State the preparation type.
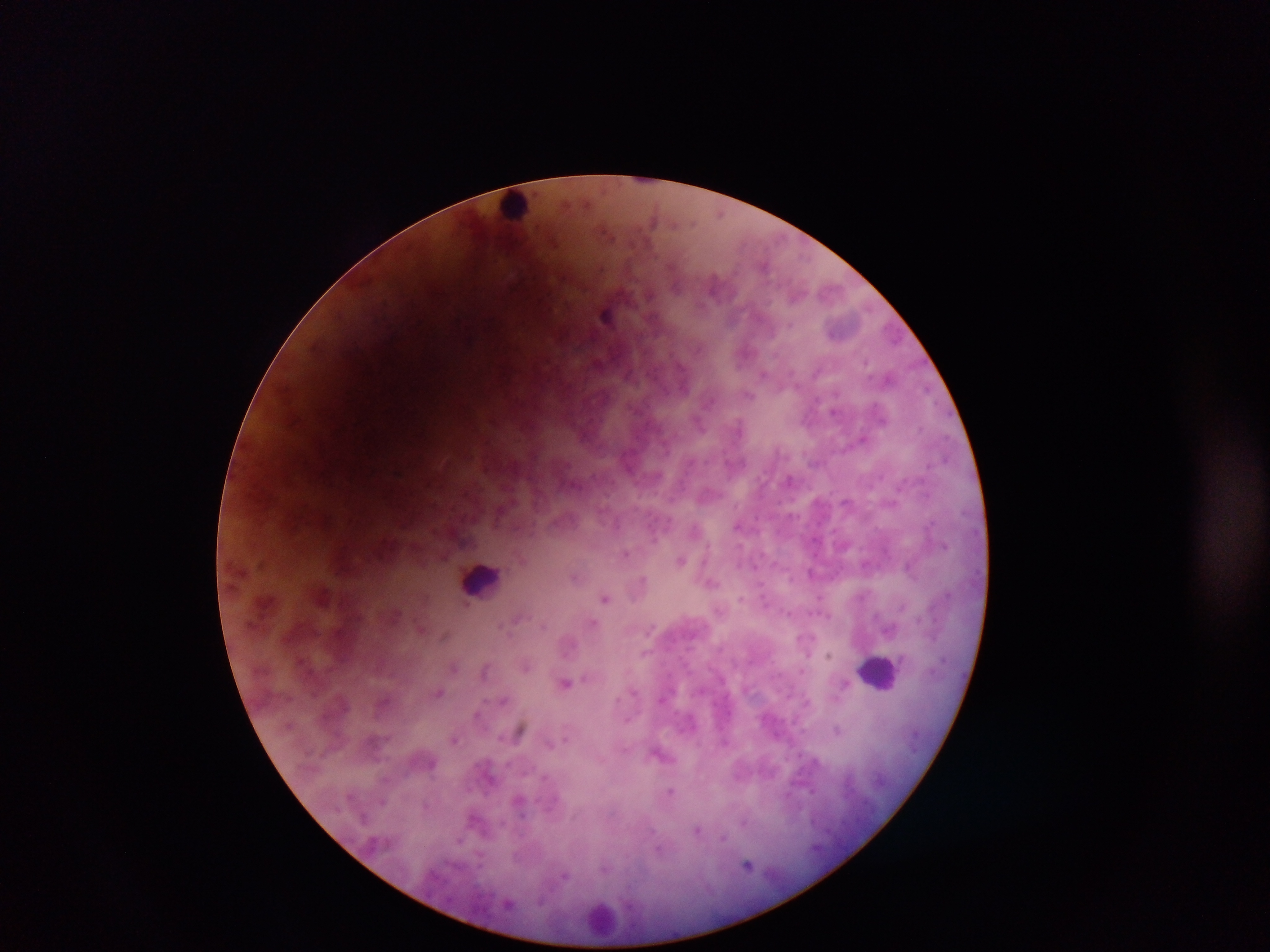
Thick blood smear.

image size = 1270×952 pixels
capture = mobile-phone photograph through a microscope
country = Ghana
field of view = single
leukocyte locations = approximate centers as x y in pixels: 516 206; 483 580; 880 673; 602 917
malaria parasite locations = approximate centers as x y in pixels: 653 221; 764 265; 714 282; 607 315; 791 324; 763 374; 749 395; 636 409; 833 411; 738 427; 863 438; 397 471; 737 525; 944 546; 626 554; 444 557; 681 559; 865 564; 756 567; 911 568; 811 573; 574 577; 642 578; 712 584; 820 596; 606 598; 466 604; 397 614; 788 614; 517 618; 593 621; 504 624; 544 626; 652 628; 420 629; 444 636; 806 654; 828 655; 526 666; 454 667; 485 670; 566 682; 439 692; 504 699; 519 730; 837 730; 455 739; 670 790; 812 791; 382 802; 364 818; 744 821; 696 830; 723 838; 460 840; 747 865; 564 876